State which parasite is depicted.
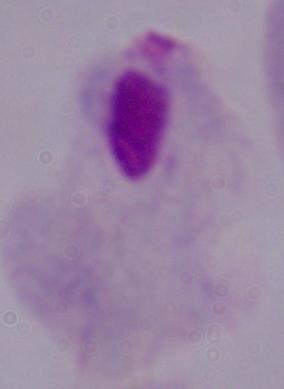
A trichomonad.

1000x magnification. Micrograph.